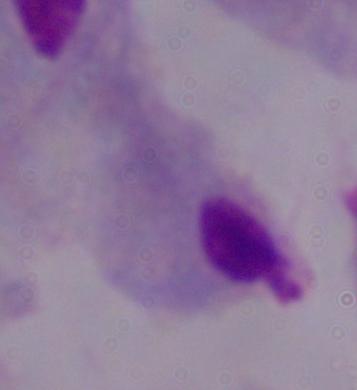

magnification: 1000x
identification: trichomonad
modality: photomicrograph